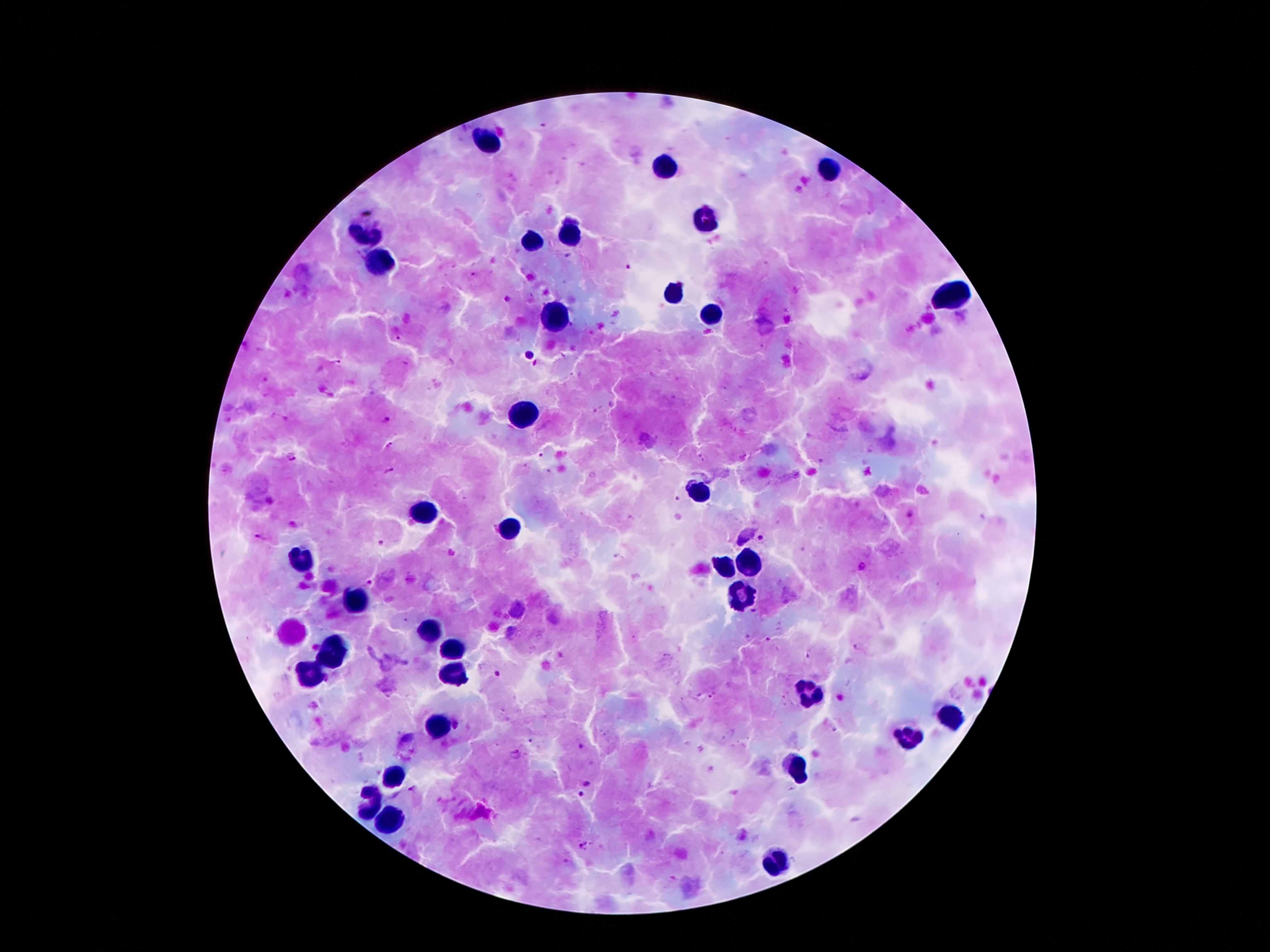
preparation: thick blood smear
stain: Giemsa
plasmodium_parasite_locations: 'approximate centers as [x, y] in pixels: [628, 267], [398, 337], [527, 354], [338, 362], [535, 362], [386, 420], [390, 445], [539, 456], [293, 459], [390, 471], [678, 498], [909, 515], [261, 538], [760, 538], [382, 542], [862, 566], [369, 582], [753, 611], [748, 635], [768, 639], [856, 646], [807, 655], [497, 674], [711, 697], [517, 752], [586, 784], [411, 788], [580, 794], [585, 845]'
image_size: 1270×952 pixels
patient_malaria_status: infected with Plasmodium falciparum
leukocyte_locations: 'approximate centers as [x, y] in pixels: [487, 143], [664, 163], [829, 169], [707, 222], [571, 233], [364, 234], [532, 241], [384, 260], [672, 294], [954, 294], [557, 317], [711, 317], [523, 413], [698, 493], [419, 512], [512, 525], [301, 563], [357, 602], [428, 634], [334, 649], [452, 650], [310, 672], [455, 674], [809, 694], [950, 715], [437, 724], [906, 735], [798, 766], [394, 772], [369, 806], [394, 818], [770, 861]'
field_of_view: single
magnification: 100x
capture: smartphone camera through the microscope eyepiece